Assess the morphology of the erythrocytes.
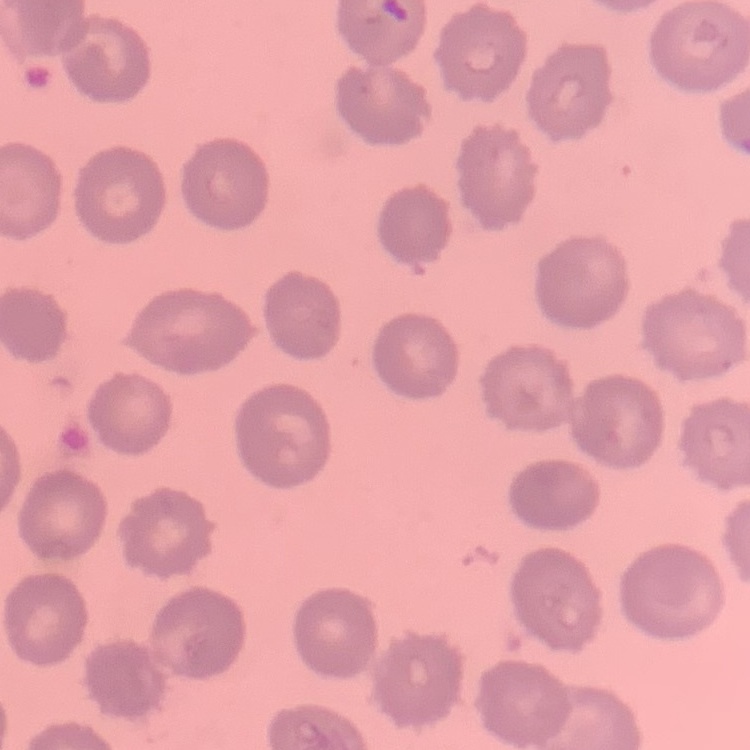

They show no rouleaux formation.

Square crop of a larger photomicrograph. Thin blood smear. Field's or Giemsa stain.